State which parasite is depicted.
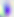

Toxoplasma gondii.

Summary:
  - Magnification: 400x
  - Modality: micrograph